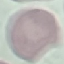

Summary:
  - Result: no malaria parasites detected
  - Image type: automatically extracted cell patch, resized to 64 × 64 pixels
  - Preparation: thin blood smear
  - Capture: smartphone camera at the microscope eyepiece
  - Stain: Giemsa